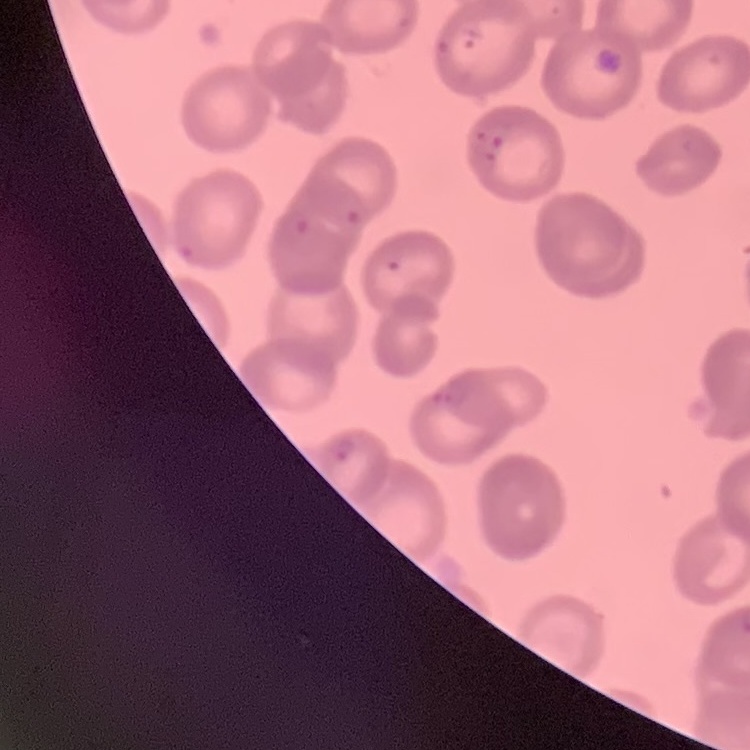

The erythrocytes exhibit no rouleaux formation. Stained with either Field's or Giemsa. Square crop of a larger photomicrograph. Thin blood smear.